Report the malaria status of this cell.
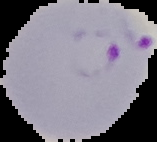

Parasitized.

From a thin blood smear. Image is 157×142 pixels. Cell region segmented out of the field of view; the surrounding area is masked to black.